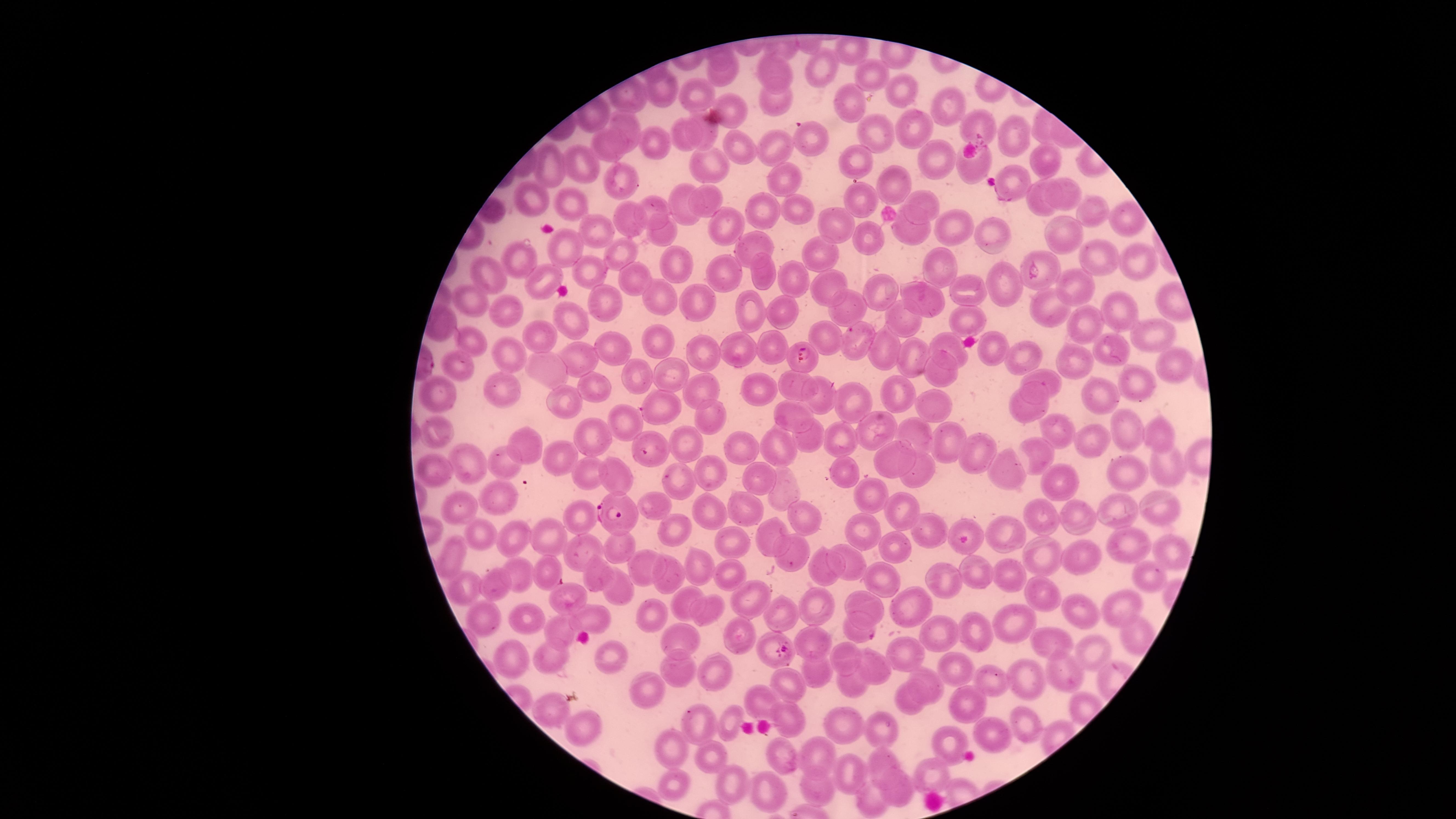
Approximate marker points, in pixels from the top-left corner.
Summary:
  - Parasitized RBCs: (x=811, y=137), (x=1037, y=272), (x=802, y=356), (x=650, y=449), (x=611, y=513), (x=548, y=570), (x=867, y=634), (x=775, y=644)
  - Uninfected RBCs: (x=724, y=71), (x=820, y=71), (x=776, y=72), (x=868, y=72), (x=700, y=89), (x=664, y=91), (x=904, y=92), (x=774, y=103), (x=847, y=103), (x=949, y=104), (x=733, y=107), (x=625, y=125), (x=977, y=125), (x=704, y=129), (x=918, y=131), (x=684, y=135), (x=877, y=135), (x=1010, y=136), (x=654, y=143), (x=607, y=147), (x=736, y=149), (x=774, y=149), (x=856, y=157), (x=927, y=157), (x=1046, y=157), (x=550, y=159), (x=973, y=161), (x=586, y=164), (x=708, y=167), (x=786, y=179), (x=623, y=181), (x=892, y=185), (x=1011, y=186), (x=1071, y=190), (x=861, y=196), (x=707, y=197), (x=1036, y=198), (x=531, y=200), (x=572, y=202), (x=681, y=203), (x=794, y=206), (x=926, y=206), (x=654, y=207), (x=765, y=211), (x=1090, y=212), (x=627, y=218), (x=723, y=219), (x=835, y=222), (x=949, y=222), (x=1127, y=222), (x=594, y=229), (x=911, y=231), (x=664, y=232), (x=1063, y=232), (x=991, y=235), (x=874, y=236), (x=752, y=244), (x=565, y=248), (x=619, y=252), (x=820, y=255), (x=1101, y=259), (x=677, y=260), (x=522, y=261), (x=1136, y=263), (x=940, y=265), (x=590, y=267), (x=727, y=267), (x=487, y=272), (x=766, y=272), (x=635, y=279), (x=793, y=279), (x=540, y=282), (x=1002, y=283), (x=1073, y=286), (x=826, y=291), (x=964, y=292), (x=463, y=294), (x=879, y=296), (x=923, y=297), (x=605, y=299), (x=665, y=299), (x=694, y=299), (x=842, y=303), (x=747, y=307), (x=1050, y=308), (x=1119, y=308), (x=499, y=310), (x=782, y=311), (x=962, y=316), (x=572, y=318), (x=900, y=319), (x=1088, y=324), (x=440, y=326), (x=1152, y=333), (x=546, y=335), (x=823, y=336), (x=856, y=339), (x=470, y=341), (x=655, y=341), (x=614, y=344), (x=945, y=344), (x=739, y=345), (x=771, y=345), (x=891, y=350), (x=995, y=350), (x=1116, y=350), (x=699, y=351), (x=579, y=354), (x=1029, y=356), (x=509, y=357), (x=915, y=357), (x=1166, y=359), (x=1072, y=363), (x=459, y=364), (x=550, y=370), (x=937, y=373), (x=670, y=376), (x=635, y=377), (x=1045, y=378), (x=1135, y=383), (x=798, y=385), (x=505, y=386), (x=755, y=386), (x=589, y=387), (x=439, y=392), (x=897, y=392), (x=698, y=393), (x=1098, y=395), (x=824, y=398), (x=565, y=402), (x=934, y=402), (x=851, y=403), (x=658, y=404), (x=1030, y=405), (x=791, y=414), (x=713, y=420), (x=625, y=421), (x=1060, y=429), (x=437, y=430), (x=872, y=430), (x=1128, y=430), (x=914, y=431), (x=1164, y=436), (x=597, y=437), (x=811, y=438), (x=524, y=439), (x=1092, y=439), (x=948, y=440), (x=841, y=441), (x=690, y=442), (x=778, y=444), (x=744, y=445), (x=975, y=450), (x=1035, y=450), (x=558, y=455), (x=895, y=456), (x=507, y=458), (x=1162, y=459), (x=473, y=463), (x=1122, y=467), (x=842, y=469), (x=1011, y=469), (x=433, y=471), (x=714, y=472), (x=757, y=473), (x=591, y=475), (x=615, y=476), (x=685, y=476), (x=922, y=476), (x=1054, y=477), (x=786, y=489), (x=872, y=493), (x=498, y=496), (x=654, y=503), (x=751, y=503), (x=1165, y=505), (x=1122, y=509), (x=459, y=511), (x=713, y=511), (x=905, y=512), (x=1038, y=514), (x=582, y=515), (x=800, y=516), (x=1077, y=519), (x=968, y=524), (x=765, y=528), (x=924, y=528), (x=864, y=530), (x=673, y=531), (x=547, y=532), (x=1006, y=536), (x=515, y=538), (x=484, y=539), (x=733, y=542), (x=1125, y=545), (x=628, y=547), (x=891, y=547), (x=581, y=548), (x=1171, y=552), (x=454, y=554), (x=1045, y=555), (x=793, y=557), (x=857, y=560), (x=1085, y=560), (x=646, y=562), (x=977, y=567), (x=824, y=568), (x=703, y=569), (x=1010, y=573), (x=518, y=575), (x=730, y=575), (x=598, y=576), (x=670, y=577), (x=1148, y=577), (x=941, y=579), (x=885, y=580), (x=497, y=584), (x=470, y=587), (x=622, y=587), (x=1038, y=594), (x=565, y=599), (x=751, y=599), (x=813, y=599), (x=689, y=602), (x=868, y=602), (x=912, y=604), (x=1122, y=606), (x=1082, y=611), (x=713, y=612), (x=590, y=615), (x=786, y=615), (x=527, y=617), (x=650, y=617), (x=489, y=618), (x=1014, y=624), (x=562, y=628), (x=975, y=628), (x=942, y=633), (x=737, y=635), (x=679, y=637), (x=816, y=641), (x=1047, y=642), (x=511, y=649), (x=846, y=651), (x=1093, y=652), (x=904, y=654), (x=608, y=655), (x=549, y=659), (x=877, y=667), (x=957, y=670), (x=817, y=671), (x=1066, y=672), (x=676, y=673), (x=717, y=676), (x=990, y=680), (x=928, y=681), (x=792, y=682), (x=1033, y=682), (x=847, y=683), (x=645, y=691), (x=904, y=701), (x=762, y=702), (x=964, y=704), (x=550, y=712), (x=789, y=716), (x=734, y=722), (x=700, y=724), (x=840, y=724), (x=1027, y=726), (x=579, y=728), (x=885, y=730), (x=995, y=736), (x=953, y=740), (x=668, y=746), (x=822, y=750), (x=784, y=754), (x=711, y=759), (x=882, y=762), (x=853, y=770), (x=930, y=774), (x=671, y=785), (x=731, y=785), (x=818, y=787), (x=767, y=790), (x=898, y=793), (x=872, y=801)
  - Stain: Giemsa
  - Species: Plasmodium falciparum
  - Preparation: thin blood film
  - Visible region: circular
  - Capture: smartphone photograph through the microscope eyepiece
  - Field of view: single
  - Image size: 1456×819 pixels
  - Presence: malaria parasites seen